Classify this cell by malaria status.
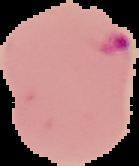

It is parasitized.

{
  "preparation": "thin blood film",
  "image_type": "segmented cell region on a black background",
  "image_size": "139×166 pixels"
}